Report the malaria status of this cell.
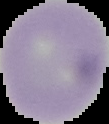

It is uninfected.

image type = cell region segmented out of the field of view; surrounding area masked to black
preparation = thin blood film
image size = 109×124 pixels